Describe the morphology of the red blood cells.
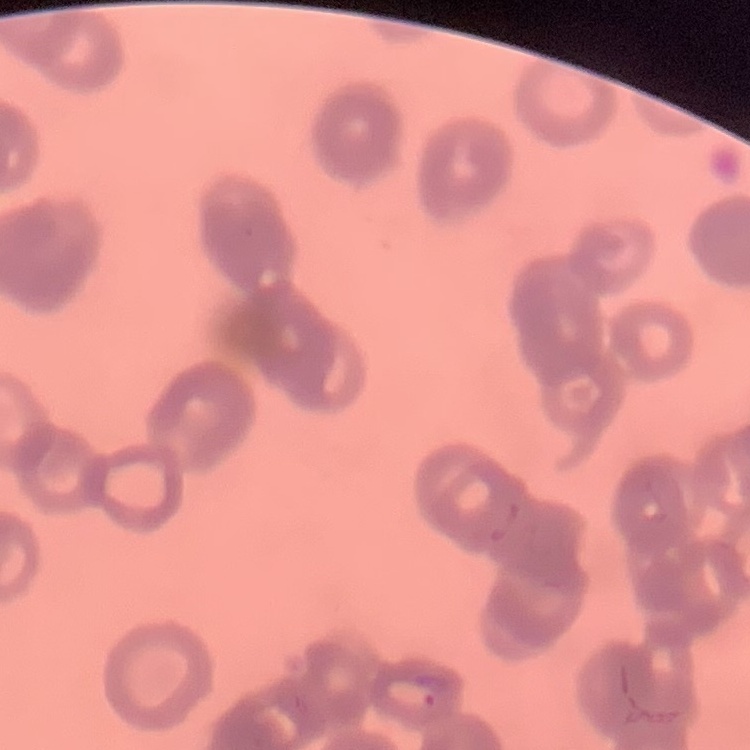
Rouleaux formation.

{
  "preparation": "thin blood smear",
  "image_type": "square crop of a larger photomicrograph",
  "stain": "Field's or Giemsa"
}